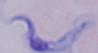
Photomicrograph. Captured at 1000x magnification. A trypanosome is shown.